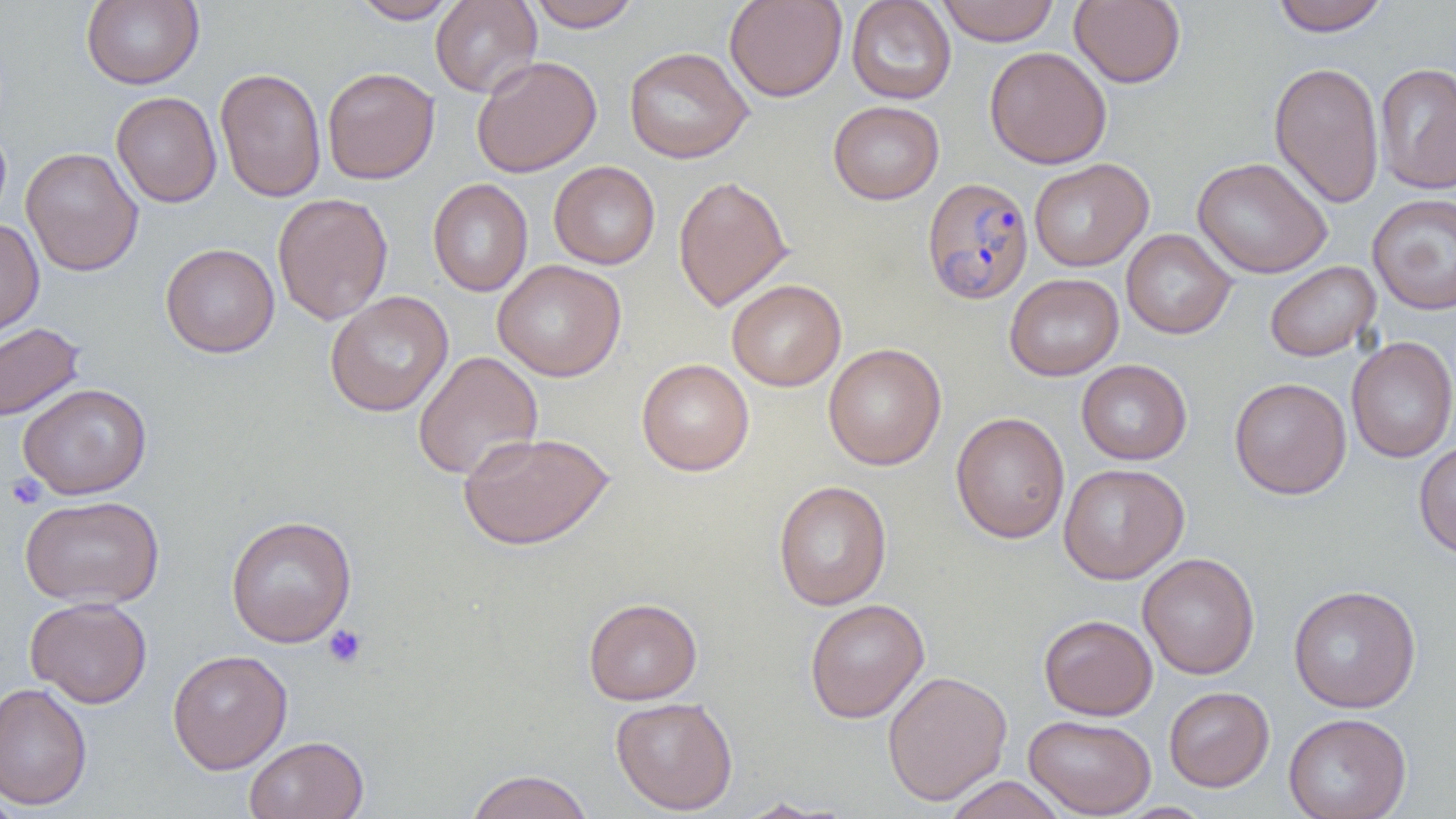
Approximate bounding boxes as (x1,y1)-(x2,y2) corner pairs in pixels. Plasmodium falciparum-infected red blood cell locations: (922,176)-(1034,305). Platelet locations: (5,472)-(47,510), (323,624)-(368,668). Uninfected red blood cell locations: (81,0)-(204,89), (350,0)-(461,24), (430,0)-(542,98), (525,0)-(641,32), (724,0)-(847,102), (846,0)-(956,104), (937,0)-(1059,46), (1069,0)-(1186,88), (1271,0)-(1389,36), (623,46)-(753,164), (984,46)-(1112,169), (471,55)-(602,178), (1269,61)-(1384,208), (1375,63)-(1456,194), (215,67)-(327,203), (322,67)-(440,185), (111,91)-(222,208), (828,100)-(944,204), (21,147)-(143,276), (1192,157)-(1332,279), (1029,158)-(1153,271), (548,161)-(660,270), (673,174)-(792,312), (428,178)-(533,297), (272,192)-(393,325), (1367,193)-(1456,315), (0,218)-(44,339), (1121,229)-(1236,339), (160,243)-(279,358), (493,259)-(626,381), (1264,261)-(1381,362), (1004,273)-(1123,381), (727,279)-(845,391), (324,291)-(454,417), (0,322)-(85,423), (1345,336)-(1456,462), (823,343)-(946,470), (413,351)-(543,481), (636,358)-(754,476), (1076,359)-(1192,465), (1229,377)-(1352,499), (18,382)-(153,500), (951,411)-(1070,543), (458,430)-(614,551), (1413,441)-(1456,559), (1059,463)-(1189,584), (773,480)-(892,611), (19,495)-(164,609), (226,515)-(357,647), (1137,552)-(1260,679), (1288,584)-(1421,713), (25,596)-(152,708), (583,597)-(702,705), (804,598)-(929,723), (1039,614)-(1157,720), (167,649)-(293,774), (882,669)-(1012,806), (0,682)-(92,811), (1163,686)-(1274,791), (610,696)-(738,815), (1283,713)-(1412,819), (1023,714)-(1156,818), (244,735)-(369,819), (465,769)-(594,819), (944,775)-(1068,819), (0,786)-(23,819), (733,797)-(840,818). Slide-level diagnosis: Plasmodium falciparum. Thin blood film. Light microscopy. Captured at 1000x magnification. Image is 1456×819 pixels. Single field of view.